Classify this cell by malaria status.
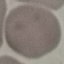
Uninfected.

capture = smartphone through the microscope eyepiece
image type = cell patch, automatically extracted from a larger field of view and resized to 64 × 64 pixels
stain = Giemsa
preparation = thin blood smear